Locate every uninfected red blood cell.
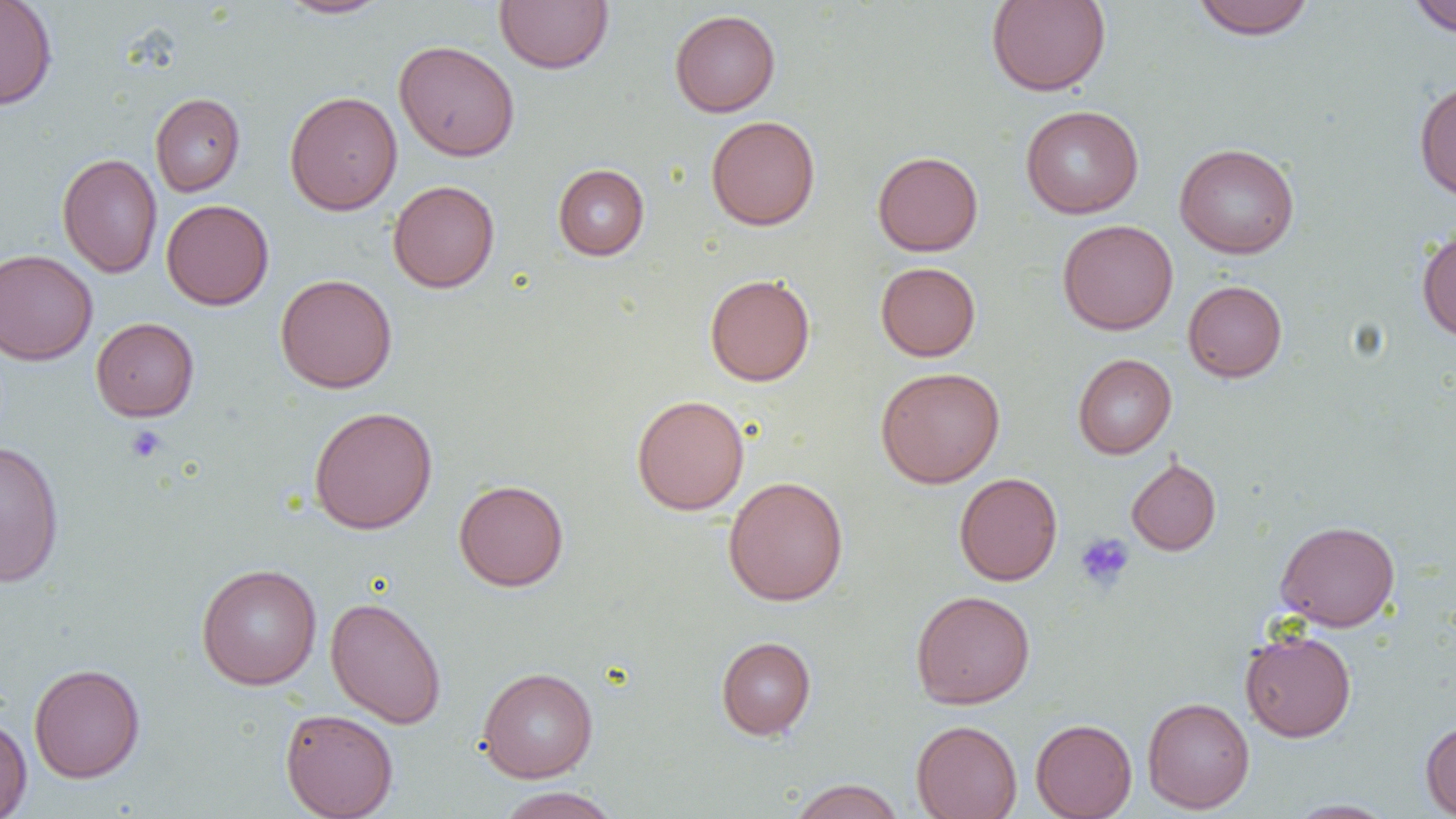

Approximate bounding boxes as named x1/y1/x2/y2 corners in pixels.
Uninfected red blood cells: (x1=0, y1=0, x2=58, y2=110), (x1=275, y1=0, x2=393, y2=19), (x1=494, y1=0, x2=613, y2=74), (x1=986, y1=0, x2=1111, y2=96), (x1=1191, y1=0, x2=1316, y2=39), (x1=1406, y1=1, x2=1456, y2=37), (x1=669, y1=9, x2=781, y2=117), (x1=393, y1=40, x2=520, y2=161), (x1=1414, y1=79, x2=1456, y2=201), (x1=284, y1=90, x2=403, y2=215), (x1=150, y1=93, x2=245, y2=197), (x1=1020, y1=105, x2=1144, y2=219), (x1=706, y1=115, x2=820, y2=231), (x1=1174, y1=142, x2=1300, y2=259), (x1=872, y1=150, x2=983, y2=256), (x1=57, y1=153, x2=163, y2=278), (x1=552, y1=164, x2=649, y2=260), (x1=388, y1=179, x2=500, y2=293), (x1=161, y1=199, x2=274, y2=310), (x1=1057, y1=219, x2=1179, y2=335), (x1=1416, y1=224, x2=1456, y2=342), (x1=0, y1=249, x2=98, y2=365), (x1=876, y1=262, x2=981, y2=361), (x1=275, y1=273, x2=398, y2=393), (x1=704, y1=273, x2=815, y2=386), (x1=1183, y1=280, x2=1287, y2=382), (x1=91, y1=317, x2=199, y2=421), (x1=1072, y1=353, x2=1176, y2=458), (x1=876, y1=366, x2=1005, y2=488), (x1=631, y1=394, x2=750, y2=515), (x1=309, y1=406, x2=438, y2=534), (x1=0, y1=440, x2=65, y2=587), (x1=1126, y1=456, x2=1221, y2=556), (x1=954, y1=472, x2=1063, y2=586), (x1=723, y1=476, x2=849, y2=606), (x1=454, y1=479, x2=569, y2=591), (x1=1275, y1=520, x2=1400, y2=631), (x1=196, y1=563, x2=322, y2=690), (x1=911, y1=590, x2=1035, y2=708), (x1=325, y1=596, x2=447, y2=729), (x1=1240, y1=629, x2=1356, y2=742), (x1=715, y1=636, x2=816, y2=740), (x1=28, y1=662, x2=145, y2=783), (x1=477, y1=666, x2=598, y2=782), (x1=1142, y1=696, x2=1255, y2=813), (x1=280, y1=708, x2=399, y2=819), (x1=0, y1=715, x2=32, y2=818), (x1=1030, y1=718, x2=1137, y2=818), (x1=911, y1=719, x2=1022, y2=819), (x1=1420, y1=719, x2=1456, y2=817), (x1=787, y1=779, x2=907, y2=819), (x1=493, y1=786, x2=623, y2=819), (x1=1285, y1=799, x2=1396, y2=818).

Summary:
  - Platelet locations: (x1=125, y1=424, x2=167, y2=463), (x1=1074, y1=533, x2=1135, y2=592)
  - Slide-level diagnosis: no evidence of blood parasites
  - Preparation: thin blood smear
  - Field of view: one of a larger specimen
  - Modality: light microscopy
  - Magnification: 1000x
  - Image size: 1456×819 pixels